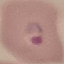

Result: malaria parasites identified. Cell patch, automatically extracted from a larger field of view and resized to 64 × 64 pixels. Thin blood smear. Giemsa-stained preparation. Acquired by smartphone through the microscope eyepiece.